Locate every blood parasite and identify its species.
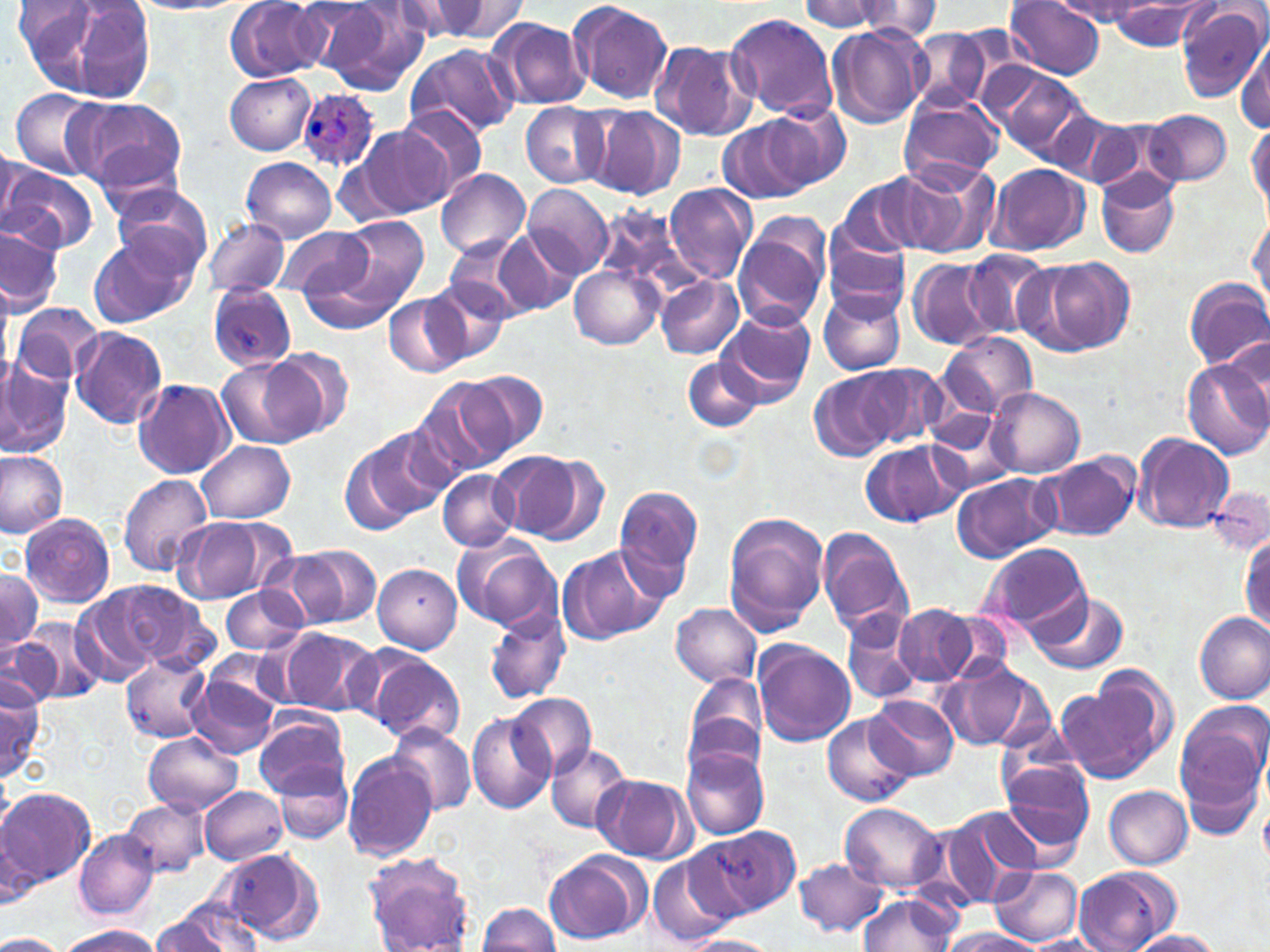

Approximate bounding boxes as (x1, y1, x2, y2) in pixels.
Plasmodium ovale-infected red blood cells: (297, 89, 377, 173).
No Plasmodium falciparum, Plasmodium malariae, Plasmodium vivax, Babesia divergens, or Trypanosoma brucei observed.

Uninfected red blood cell locations: (36, 0, 158, 104), (314, 0, 429, 96), (567, 0, 675, 104), (1054, 0, 1149, 24), (225, 1, 328, 83), (390, 1, 484, 39), (426, 1, 529, 41), (795, 1, 898, 33), (851, 1, 944, 39), (14, 2, 98, 73), (1008, 2, 1105, 77), (1109, 2, 1212, 51), (1174, 5, 1269, 102), (727, 13, 837, 118), (487, 19, 589, 107), (826, 26, 930, 129), (908, 28, 996, 112), (649, 39, 757, 141), (1236, 39, 1269, 132), (406, 48, 514, 139), (989, 66, 1088, 161), (225, 73, 314, 154), (10, 87, 103, 178), (900, 93, 1004, 184), (68, 96, 189, 200), (767, 102, 851, 190), (397, 103, 487, 202), (522, 103, 610, 187), (581, 106, 685, 198), (1045, 108, 1141, 188), (1142, 108, 1232, 187), (719, 116, 816, 205), (1077, 117, 1169, 194), (1247, 120, 1269, 213), (350, 125, 453, 221), (0, 150, 31, 234), (240, 156, 337, 243), (887, 163, 997, 261), (2, 164, 99, 255), (988, 164, 1088, 256), (437, 168, 530, 260), (1095, 170, 1180, 258), (835, 178, 927, 262), (520, 183, 614, 281), (108, 184, 215, 285), (664, 185, 755, 286), (591, 206, 706, 303), (1248, 213, 1270, 314), (732, 215, 832, 331), (203, 218, 291, 298), (312, 218, 431, 322), (278, 225, 374, 300), (820, 225, 913, 321), (0, 226, 63, 313), (495, 230, 582, 315), (89, 236, 187, 328), (444, 236, 535, 323), (962, 250, 1050, 337), (1017, 257, 1131, 356), (908, 258, 999, 351), (569, 265, 662, 349), (656, 276, 744, 359), (426, 278, 512, 363), (1184, 278, 1270, 371), (207, 283, 296, 373), (817, 289, 906, 376), (384, 291, 470, 376), (12, 303, 102, 385), (716, 307, 816, 407), (68, 326, 168, 430), (939, 331, 1038, 420), (1228, 334, 1269, 414), (262, 346, 355, 440), (216, 356, 316, 448), (683, 357, 763, 434), (0, 359, 71, 458), (1183, 360, 1270, 461), (852, 364, 948, 451), (455, 371, 548, 459), (808, 371, 898, 462), (411, 377, 512, 479), (133, 378, 233, 479), (986, 387, 1085, 479), (923, 408, 1018, 492), (339, 428, 451, 535), (1133, 433, 1234, 531), (860, 439, 966, 529), (199, 441, 296, 523), (0, 451, 67, 537), (497, 453, 591, 541), (1041, 453, 1138, 540), (438, 469, 518, 550), (951, 472, 1059, 564), (117, 474, 212, 578), (614, 485, 703, 593), (1206, 486, 1270, 555), (19, 513, 116, 607), (724, 515, 828, 637), (176, 518, 274, 603), (818, 526, 915, 637), (1239, 531, 1269, 635), (453, 536, 562, 634), (978, 542, 1091, 640), (288, 545, 381, 628), (560, 546, 662, 644), (373, 564, 462, 654), (0, 567, 40, 655), (81, 579, 207, 678), (218, 584, 309, 656), (1029, 591, 1129, 675), (671, 603, 762, 688), (484, 604, 572, 705), (893, 605, 979, 687), (840, 609, 925, 706), (1195, 612, 1269, 703), (10, 618, 106, 704), (282, 627, 378, 715), (0, 634, 61, 705), (751, 639, 856, 745), (202, 649, 285, 722), (361, 651, 466, 747), (120, 653, 211, 744), (936, 660, 1045, 752), (190, 673, 278, 758), (686, 673, 768, 771), (1059, 673, 1174, 782), (0, 682, 45, 784), (510, 693, 597, 778), (870, 695, 959, 780), (1174, 697, 1270, 822), (466, 711, 554, 813), (822, 712, 913, 807), (252, 713, 349, 798), (387, 723, 477, 817), (142, 732, 243, 816), (546, 743, 633, 833), (681, 747, 769, 839), (341, 752, 439, 862), (275, 758, 355, 845), (996, 759, 1095, 862), (591, 774, 693, 863), (1104, 785, 1192, 868), (198, 786, 289, 865), (0, 787, 96, 885), (121, 799, 208, 877), (840, 802, 946, 893), (939, 804, 1041, 904), (1, 815, 44, 909), (693, 828, 793, 921), (74, 830, 158, 920), (217, 849, 324, 945), (545, 851, 649, 944), (649, 852, 736, 947), (364, 853, 475, 951), (793, 857, 891, 938), (989, 865, 1083, 946), (1075, 867, 1180, 951), (857, 894, 958, 951), (477, 901, 559, 951), (151, 905, 256, 952), (55, 924, 163, 952), (939, 927, 1046, 952), (1128, 930, 1222, 951), (0, 934, 69, 951), (1019, 935, 1106, 952), (686, 936, 780, 952). Slide-level diagnosis: Plasmodium ovale. Thin blood smear. Image is 1270×952 pixels. Single field of view. 1000x magnification. May-Grünwald-Giemsa stain. Light microscopy.